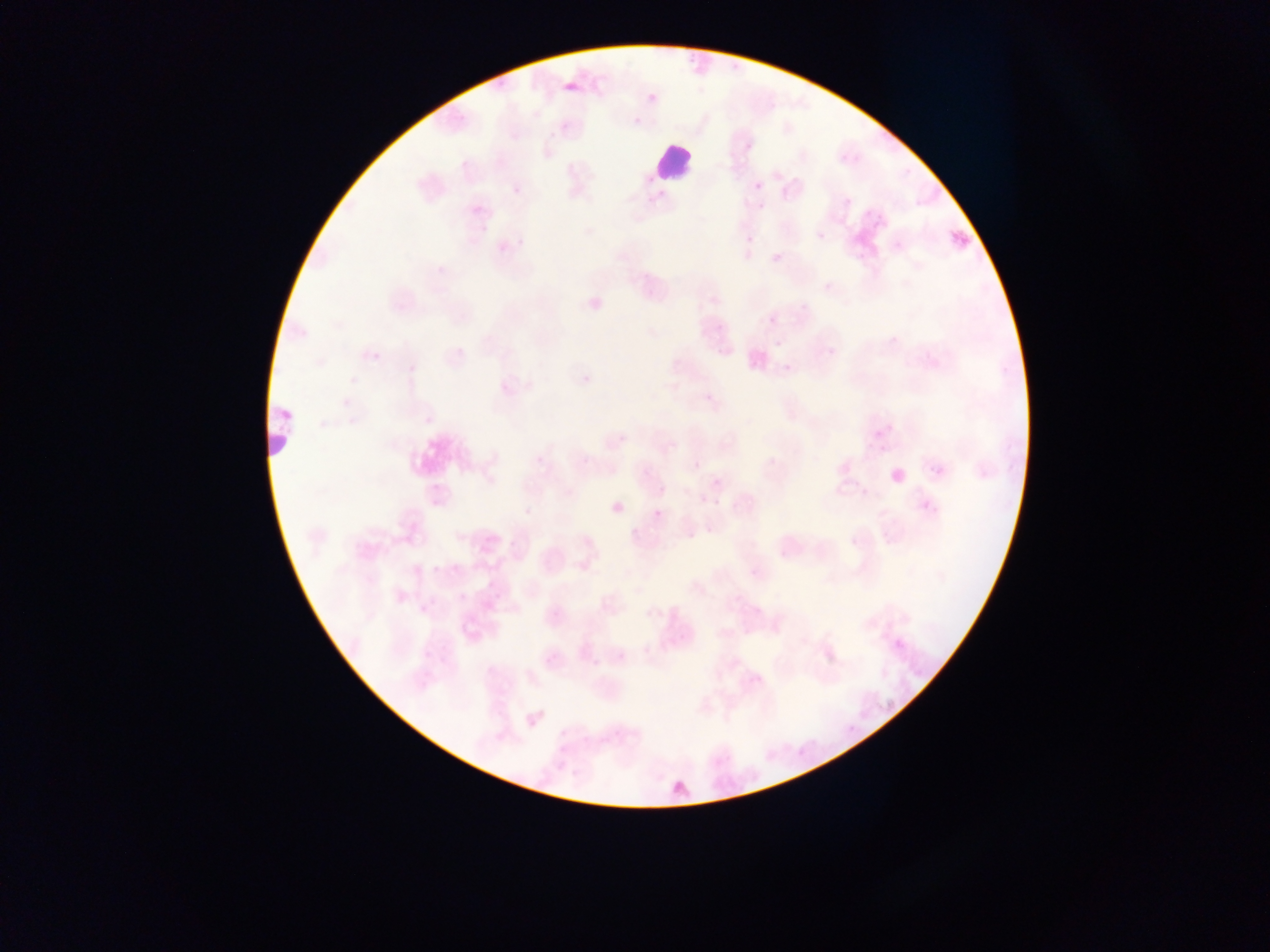
leukocyte locations = approximate bounding boxes as left top right bottom in pixels: 654 141 692 179; 267 405 296 451
image size = 1270×952 pixels
country = Ghana
preparation = thin blood film
capture = mobile-phone photograph through a microscope
malaria parasite locations = approximate bounding boxes as left top right bottom in pixels: 565 83 578 93; 752 176 764 187; 915 200 922 208; 747 224 764 243; 816 231 826 241; 951 231 969 249; 824 282 833 290; 764 305 780 326; 776 340 784 348; 456 348 466 358; 784 364 791 372; 619 433 628 442; 692 462 700 470; 711 479 720 487; 658 487 666 496; 862 488 871 497; 698 493 708 502; 921 499 929 510; 653 509 662 519; 705 525 712 533; 688 531 697 539; 849 538 857 547; 509 540 517 548; 579 561 588 571; 486 601 495 611; 553 608 564 621; 616 650 626 661; 592 658 602 667; 560 729 569 737; 602 737 611 745
field of view = single